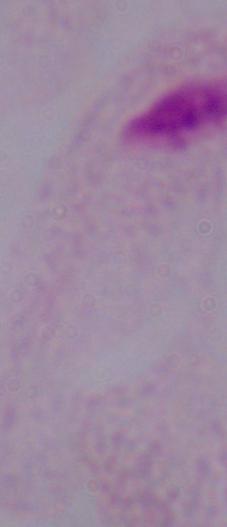
magnification = 1000x
modality = micrograph
identification = trichomonad